Locate and identify every blood parasite.
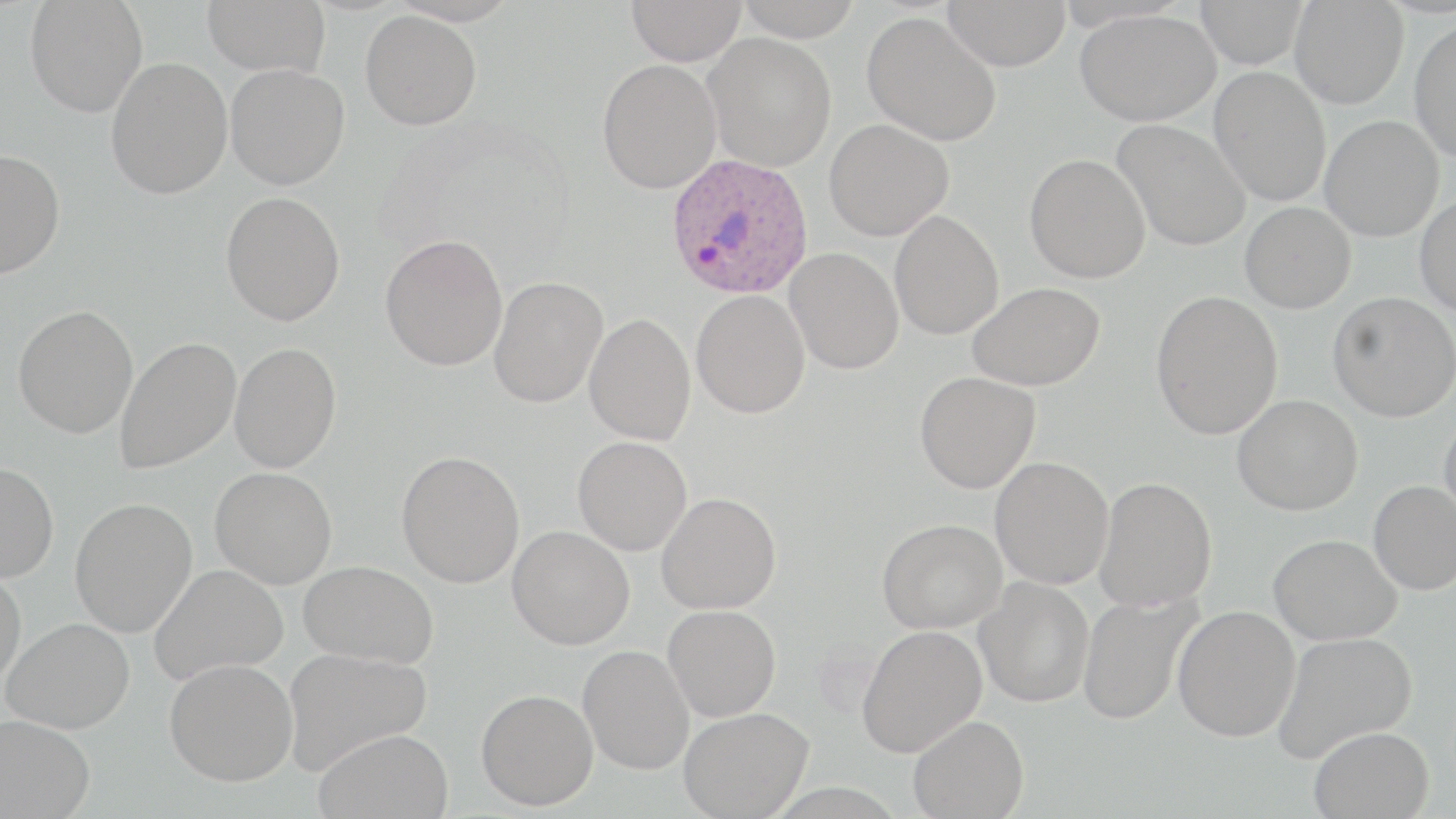
Approximate bounding boxes as [x1, y1, x2, y2] in pixels.
Plasmodium ovale-infected red blood cells: [665, 152, 814, 300].
No Plasmodium falciparum, Plasmodium malariae, Plasmodium vivax, Babesia divergens, or Trypanosoma brucei observed.

Uninfected red blood cell locations: [25, 0, 148, 117], [202, 0, 331, 76], [626, 0, 747, 66], [734, 0, 863, 41], [942, 0, 1071, 71], [1194, 0, 1308, 69], [1290, 0, 1408, 109], [1075, 8, 1221, 126], [360, 10, 482, 130], [862, 12, 1001, 146], [1409, 17, 1456, 162], [703, 32, 836, 172], [106, 57, 233, 199], [597, 59, 721, 193], [225, 63, 350, 190], [1209, 67, 1331, 207], [1320, 115, 1444, 241], [824, 119, 953, 241], [1112, 119, 1251, 251], [0, 149, 65, 279], [1025, 154, 1150, 284], [220, 191, 345, 326], [1414, 194, 1456, 317], [1240, 201, 1356, 313], [889, 210, 1004, 340], [380, 233, 508, 372], [784, 248, 903, 374], [489, 275, 608, 408], [967, 282, 1105, 391], [691, 290, 810, 418], [1150, 290, 1283, 440], [1328, 291, 1456, 422], [13, 304, 138, 439], [584, 313, 695, 445], [114, 337, 241, 475], [229, 343, 341, 473], [915, 371, 1040, 493], [1232, 394, 1363, 515], [1438, 413, 1456, 526], [573, 436, 692, 555], [396, 450, 525, 588], [989, 457, 1114, 590], [0, 462, 59, 583], [210, 467, 337, 589], [1095, 477, 1217, 611], [1368, 480, 1456, 595], [656, 492, 781, 613], [70, 497, 198, 638], [877, 518, 1006, 634], [507, 526, 635, 650], [1269, 533, 1401, 644], [299, 560, 439, 668], [149, 563, 288, 685], [0, 570, 26, 691], [974, 577, 1094, 707], [1077, 592, 1203, 725], [663, 605, 781, 721], [1172, 605, 1300, 742], [1, 617, 135, 734], [857, 625, 987, 757], [1273, 631, 1417, 762], [577, 644, 695, 775], [282, 647, 432, 775], [164, 658, 298, 786], [476, 688, 598, 810], [679, 707, 813, 818], [0, 715, 96, 819], [908, 715, 1029, 818], [1309, 726, 1435, 818], [314, 727, 454, 819]. Slide-level diagnosis: Plasmodium ovale. 1000x magnification. Thin blood smear. Optical microscopy. Single field of view. Image is 1456×819 pixels. May-Grünwald-Giemsa-stained preparation.